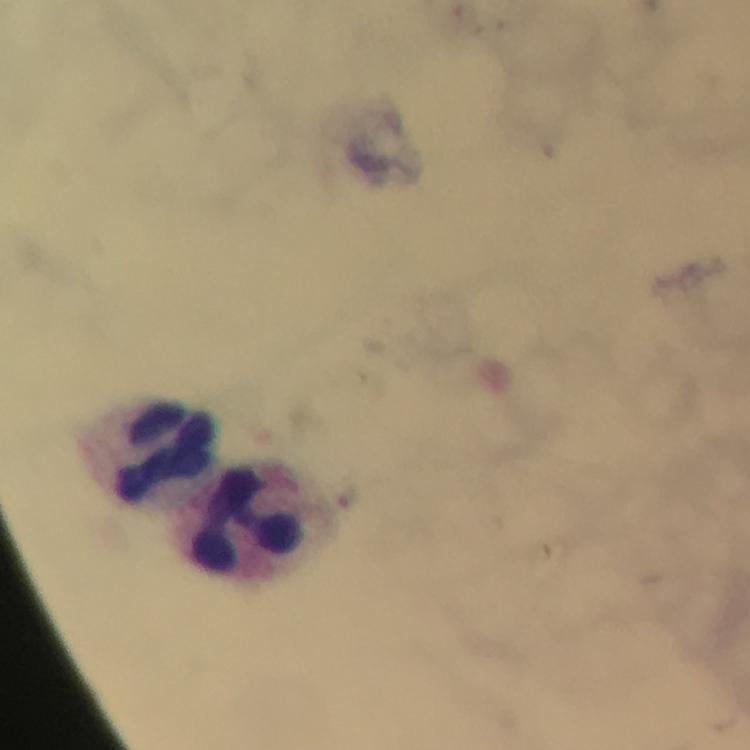

Approximate centers as (x, y) in pixels.
Summary:
  - Leukocyte locations: (162, 450), (247, 519)
  - Preparation: thick blood smear
  - Context: from a diagnostic examination for malaria
  - Image size: 750×750 pixels
  - Magnification: 100x
  - Stain: Giemsa
  - Capture: smartphone camera through the microscope
  - Malaria parasites: none detected
  - Cropped from: a single field of view
  - Immersion oil: used